Outline each blood parasite and name the species.
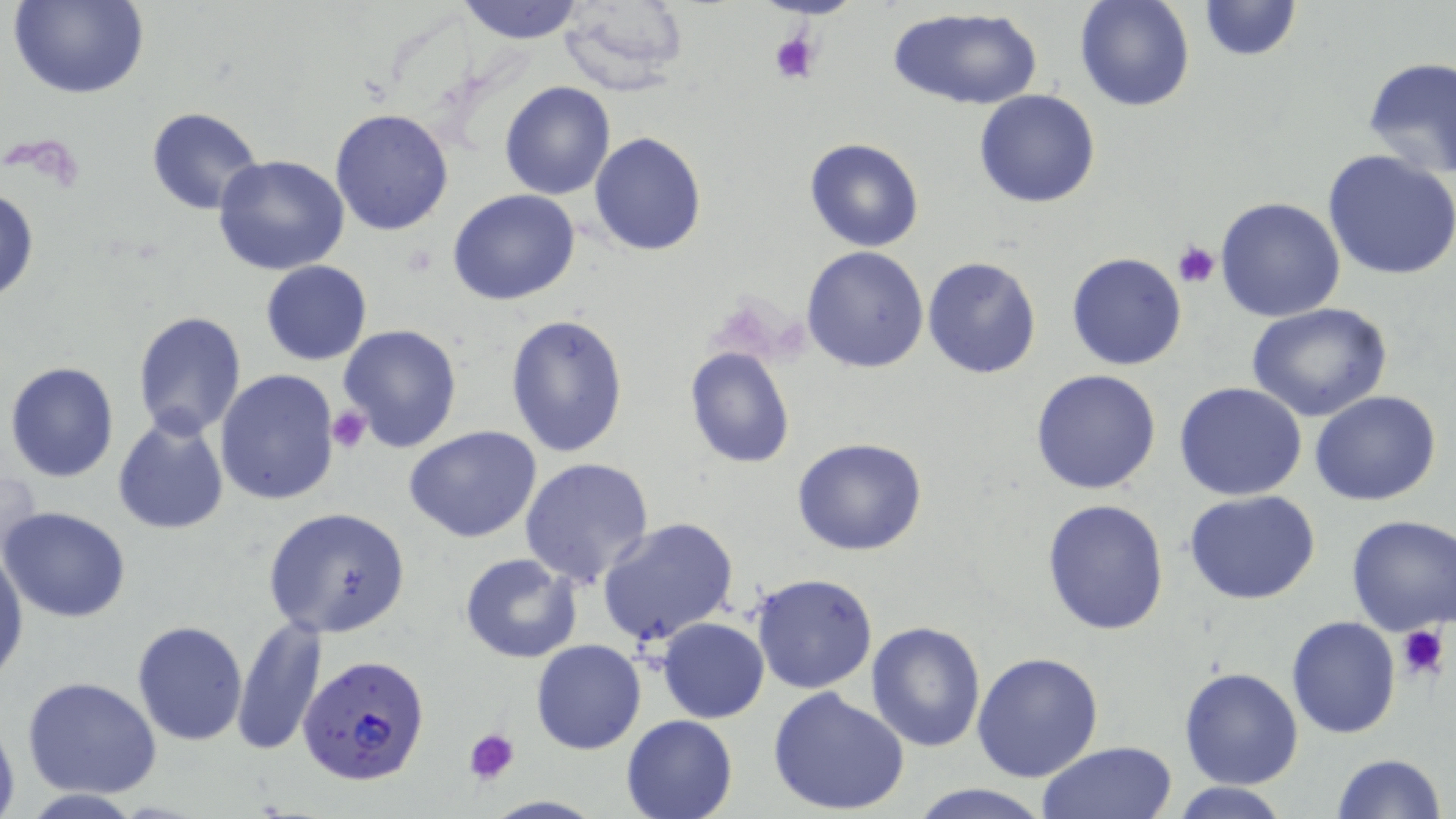

Approximate bounding boxes as [x1, y1, x2, y2] in pixels.
Plasmodium falciparum-infected red blood cells: [298, 653, 430, 787].
No Plasmodium ovale, Plasmodium malariae, Plasmodium vivax, Babesia divergens, or Trypanosoma brucei observed.

Summary:
  - Uninfected red blood cell locations: [10, 0, 150, 100], [455, 0, 587, 45], [1074, 0, 1196, 112], [1194, 0, 1304, 63], [556, 1, 691, 95], [887, 8, 1044, 111], [1361, 55, 1456, 181], [499, 82, 616, 200], [974, 89, 1102, 208], [146, 106, 265, 216], [331, 107, 455, 235], [589, 132, 707, 256], [805, 138, 924, 253], [1323, 150, 1456, 281], [212, 154, 350, 275], [0, 185, 39, 305], [447, 189, 581, 307], [1215, 197, 1346, 321], [801, 246, 931, 373], [1065, 252, 1187, 371], [922, 255, 1042, 379], [260, 260, 372, 365], [1248, 305, 1392, 423], [133, 312, 247, 440], [505, 313, 632, 458], [337, 324, 464, 452], [685, 346, 795, 468], [4, 362, 120, 483], [215, 368, 342, 506], [1029, 370, 1161, 496], [1174, 382, 1308, 501], [1310, 390, 1441, 507], [111, 416, 230, 535], [404, 425, 543, 543], [792, 436, 927, 556], [519, 457, 656, 589], [1, 462, 43, 563], [1185, 491, 1321, 606], [1041, 497, 1169, 635], [261, 506, 412, 638], [1, 508, 131, 622], [1344, 513, 1456, 637], [595, 516, 740, 650], [0, 545, 28, 687], [459, 553, 582, 663], [750, 572, 879, 694], [231, 615, 326, 756], [656, 617, 770, 722], [1287, 617, 1400, 738], [132, 620, 248, 745], [865, 621, 985, 753], [532, 639, 646, 754], [971, 651, 1104, 783], [1179, 667, 1304, 790], [22, 675, 162, 799], [767, 686, 913, 817], [0, 713, 20, 819], [620, 713, 739, 819], [1037, 742, 1178, 819], [1330, 752, 1446, 818], [904, 782, 1056, 819], [1169, 782, 1293, 818]
  - Platelet locations: [767, 29, 823, 87], [1174, 240, 1221, 287], [328, 405, 372, 454], [1395, 623, 1450, 684], [463, 726, 522, 785]
  - Slide-level diagnosis: Plasmodium falciparum
  - Magnification: 1000x
  - Field of view: single
  - Modality: light microscopy
  - Preparation: thin blood film
  - Image size: 1456×819 pixels
  - Stain: May-Grünwald-Giemsa